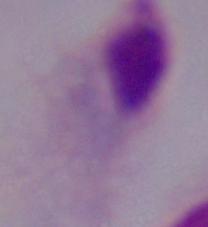

Summary:
  - Modality: micrograph
  - Identification: trichomonad
  - Magnification: 1000x